Locate and identify every blood parasite.
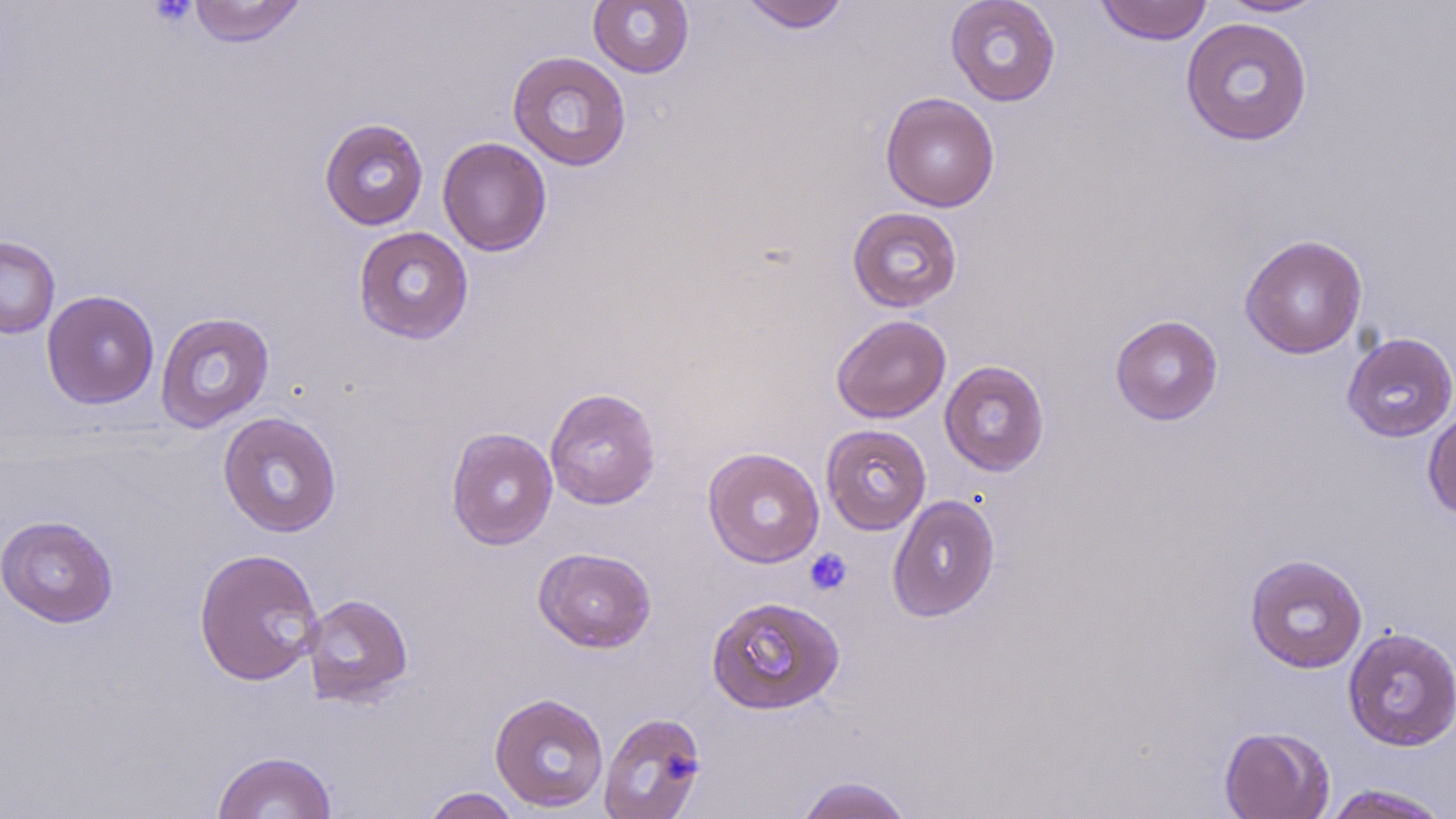
No blood parasites seen.

Approximate bounding boxes as [x1, y1, x2, y2] in pixels. Platelet locations: [148, 0, 199, 28], [804, 548, 852, 596]. Uninfected red blood cell locations: [188, 0, 308, 47], [740, 0, 851, 33], [944, 0, 1062, 106], [588, 1, 695, 78], [1095, 1, 1213, 45], [1219, 1, 1327, 17], [1180, 16, 1313, 147], [507, 51, 632, 171], [880, 92, 1000, 212], [319, 118, 429, 230], [437, 136, 552, 256], [847, 206, 963, 313], [353, 226, 474, 344], [1239, 234, 1368, 359], [0, 235, 60, 338], [41, 289, 160, 409], [155, 311, 275, 432], [831, 314, 951, 423], [1110, 314, 1223, 425], [1341, 331, 1456, 442], [939, 360, 1050, 477], [544, 387, 662, 510], [1422, 408, 1456, 520], [217, 411, 343, 537], [821, 424, 932, 535], [445, 427, 558, 550], [702, 447, 825, 568], [887, 494, 1001, 622], [0, 515, 119, 627], [193, 547, 324, 686], [533, 547, 657, 653], [1244, 553, 1368, 673], [302, 593, 413, 707], [705, 595, 845, 715], [1343, 626, 1456, 751], [489, 692, 609, 812], [598, 711, 707, 819], [1219, 725, 1334, 819], [211, 750, 339, 818], [794, 775, 916, 819], [1320, 783, 1452, 818], [421, 787, 521, 818]. Slide-level diagnosis: negative for blood parasites. Captured at 1000x magnification. Single field of view. Thin blood film. May-Grünwald-Giemsa-stained preparation. Light microscopy. Image is 1456×819 pixels.